Give the preparation type.
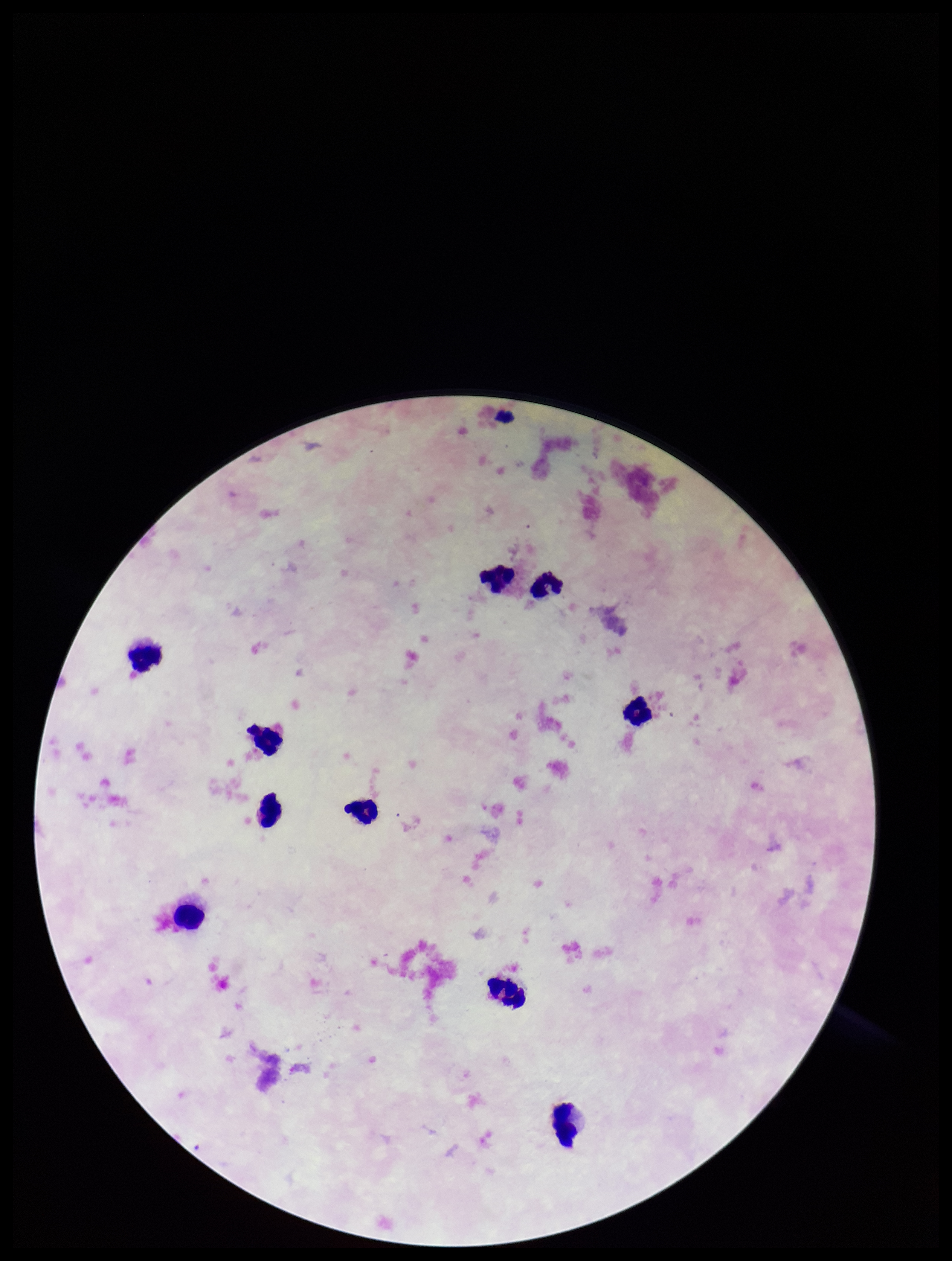
It is a thick blood smear.

Summary:
  - Parasite count: 0
  - Capture: smartphone photograph through the microscope eyepiece
  - Field of view: one from this slide
  - Leukocyte count: 10
  - Patient malaria status: negative
  - Image size: 952×1261 pixels
  - Plasmodium parasites: none seen
  - Stain: Giemsa